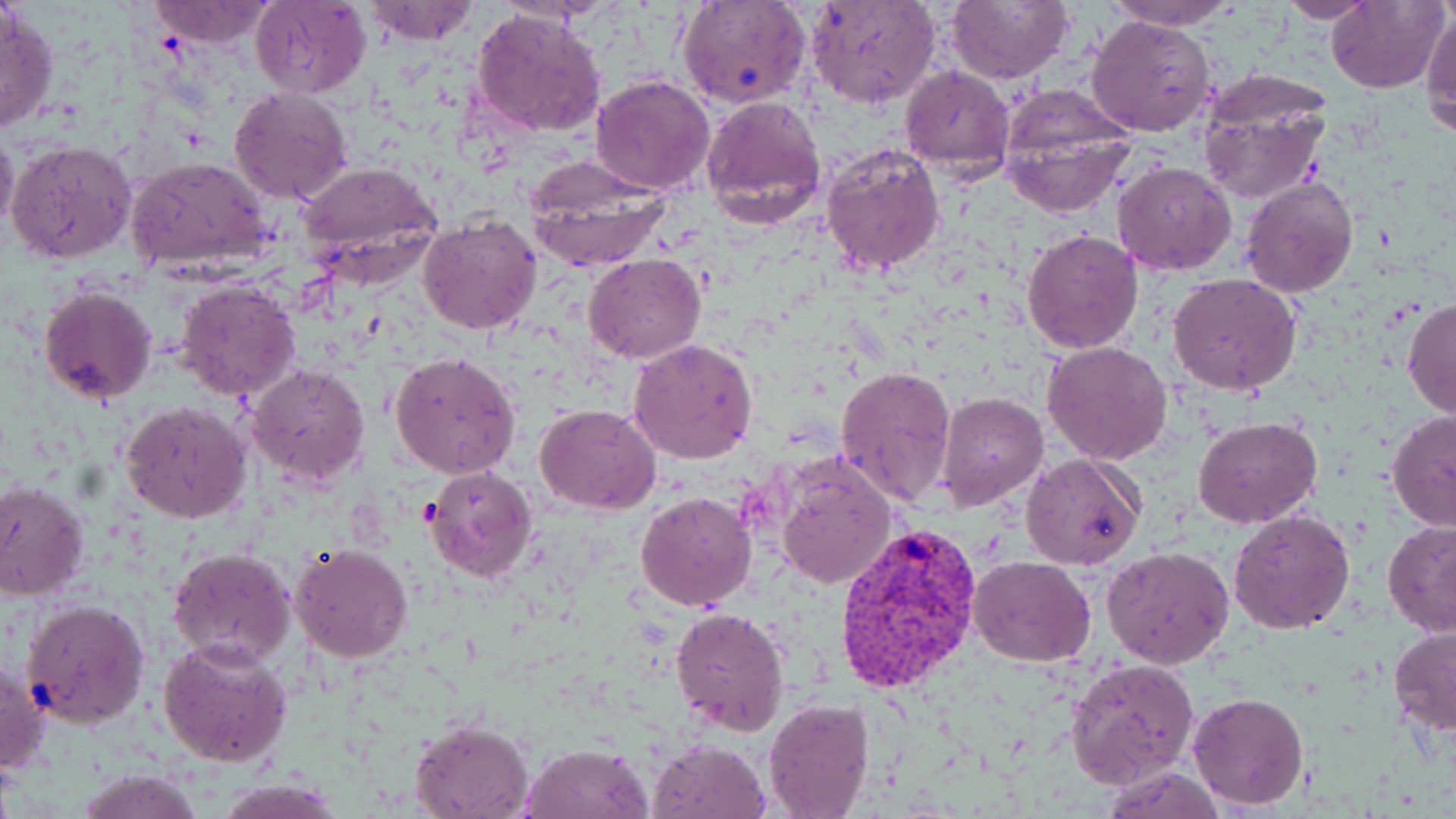
Summary:
  - Coordinate format: approximate bounding boxes as (x1,y1)-(x2,y2) corner pairs in pixels
  - Uninfected red blood cell locations: (250,0)-(369,98), (358,0)-(480,45), (805,0)-(942,110), (944,0)-(1073,84), (1101,0)-(1245,30), (1275,0)-(1380,21), (1328,0)-(1449,94), (144,1)-(277,49), (679,1)-(811,110), (1,4)-(59,135), (1421,8)-(1456,135), (470,10)-(608,138), (1086,15)-(1215,136), (898,65)-(1015,176), (588,73)-(716,194), (1196,77)-(1330,205), (997,86)-(1138,216), (230,87)-(352,206), (700,97)-(829,224), (0,125)-(19,236), (6,138)-(137,265), (820,141)-(946,276), (125,155)-(274,273), (295,160)-(443,280), (1112,160)-(1237,275), (527,163)-(671,270), (1241,176)-(1359,297), (418,212)-(542,335), (1022,228)-(1143,354), (584,253)-(706,363), (1167,273)-(1301,395), (175,280)-(302,401), (40,284)-(159,405), (1402,297)-(1456,420), (628,337)-(758,465), (1042,341)-(1173,465), (391,351)-(520,480), (246,362)-(370,490), (835,364)-(957,510), (936,394)-(1050,510), (121,401)-(252,523), (535,403)-(660,514), (1385,409)-(1456,532), (1193,416)-(1323,531), (1021,452)-(1147,570), (776,460)-(895,590), (424,467)-(539,582), (0,481)-(89,602), (636,492)-(757,610), (1228,507)-(1356,632), (1382,518)-(1456,637), (290,544)-(415,663), (1103,545)-(1234,668), (166,547)-(296,667), (968,556)-(1095,667), (20,598)-(150,729), (670,606)-(790,738), (1388,626)-(1456,736), (158,636)-(294,769), (1066,657)-(1197,786), (0,661)-(49,775), (1187,691)-(1309,809), (762,698)-(876,819), (408,720)-(534,819), (648,740)-(770,819), (520,741)-(653,818), (1099,764)-(1228,818), (72,768)-(202,819), (212,779)-(344,818)
  - Plasmodium vivax-infected red blood cell locations: (833,521)-(981,694)
  - Slide-level diagnosis: Plasmodium vivax
  - Image size: 1456×819 pixels
  - Magnification: 1000x
  - Modality: optical microscopy
  - Stain: May-Grünwald-Giemsa
  - Field of view: single
  - Preparation: thin blood smear